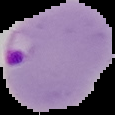

Summary:
  - Result: Plasmodium parasites detected
  - Image size: 115×115 pixels
  - Preparation: thin blood smear
  - Image type: cell region segmented out of the field of view; surrounding area masked to black